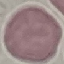

Malaria status: uninfected. Giemsa-stained preparation. Thin blood film. Cell patch, automatically extracted from a larger field of view and resized to 64 × 64 pixels. Photographed with a smartphone camera at the microscope eyepiece.